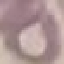

Result: no malaria parasites seen. Acquired by smartphone through the microscope eyepiece. Thin blood smear. Giemsa-stained preparation. Automatically extracted cell patch, resized to 64 × 64 pixels.